Describe the morphology of the red blood cells.
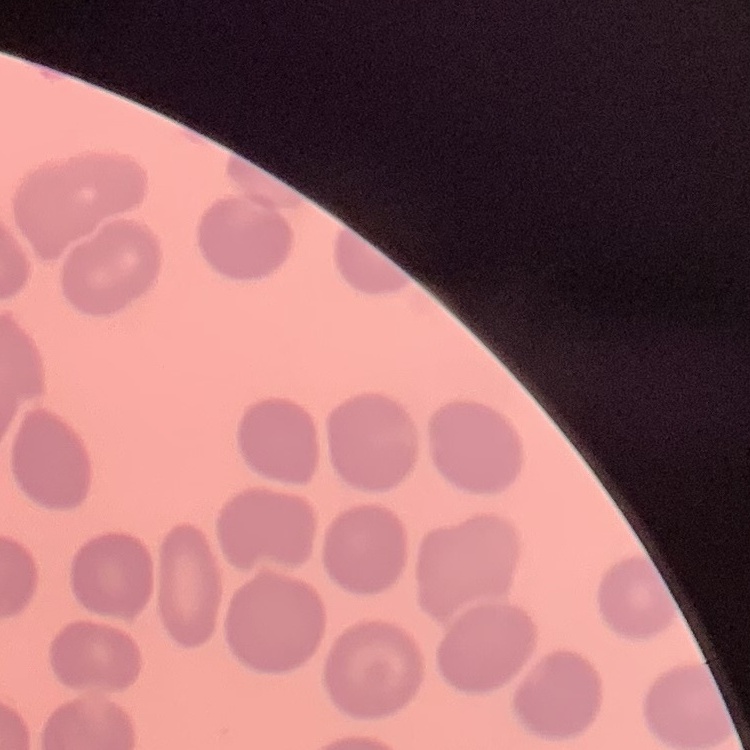

They show no rouleaux formation.

One tile cut from a larger photomicrograph. Field's or Giemsa stain. Thin blood film.